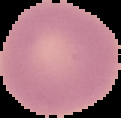

Summary:
  - Image size: 121×118 pixels
  - Image type: segmented cell region with the area outside set to black
  - Result: negative for Plasmodium parasites
  - Preparation: thin blood smear